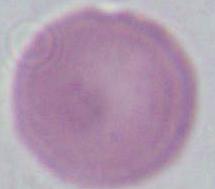
Summary:
  - Identification: erythrocyte
  - Modality: micrograph
  - Magnification: 1000x